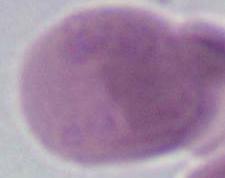
modality = photomicrograph
identification = red blood cell
magnification = 1000x